Assess the morphology of the erythrocytes.
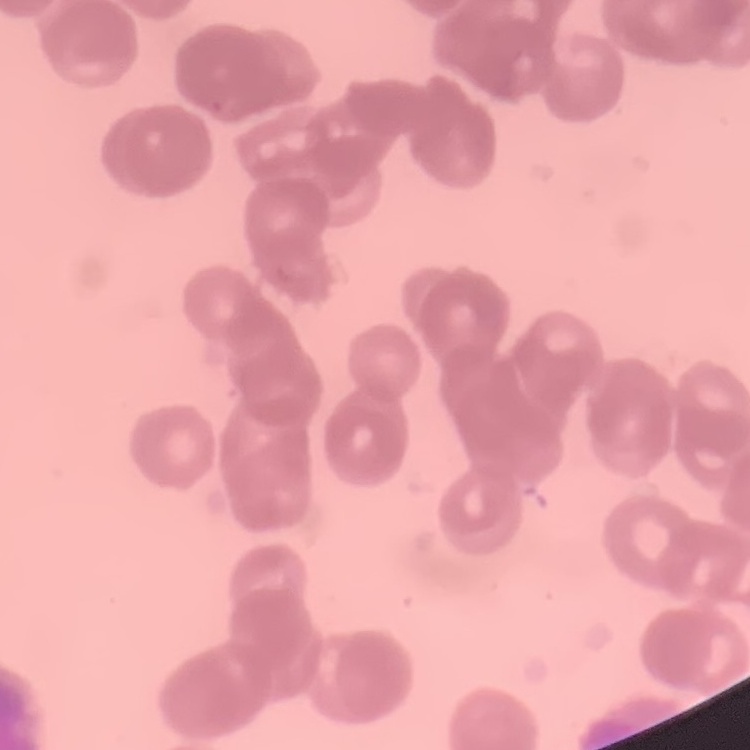

They show rouleaux formation.

stain = Field's or Giemsa
preparation = thin blood smear
image type = one tile cut from a larger photomicrograph